Locate and identify every blood parasite.
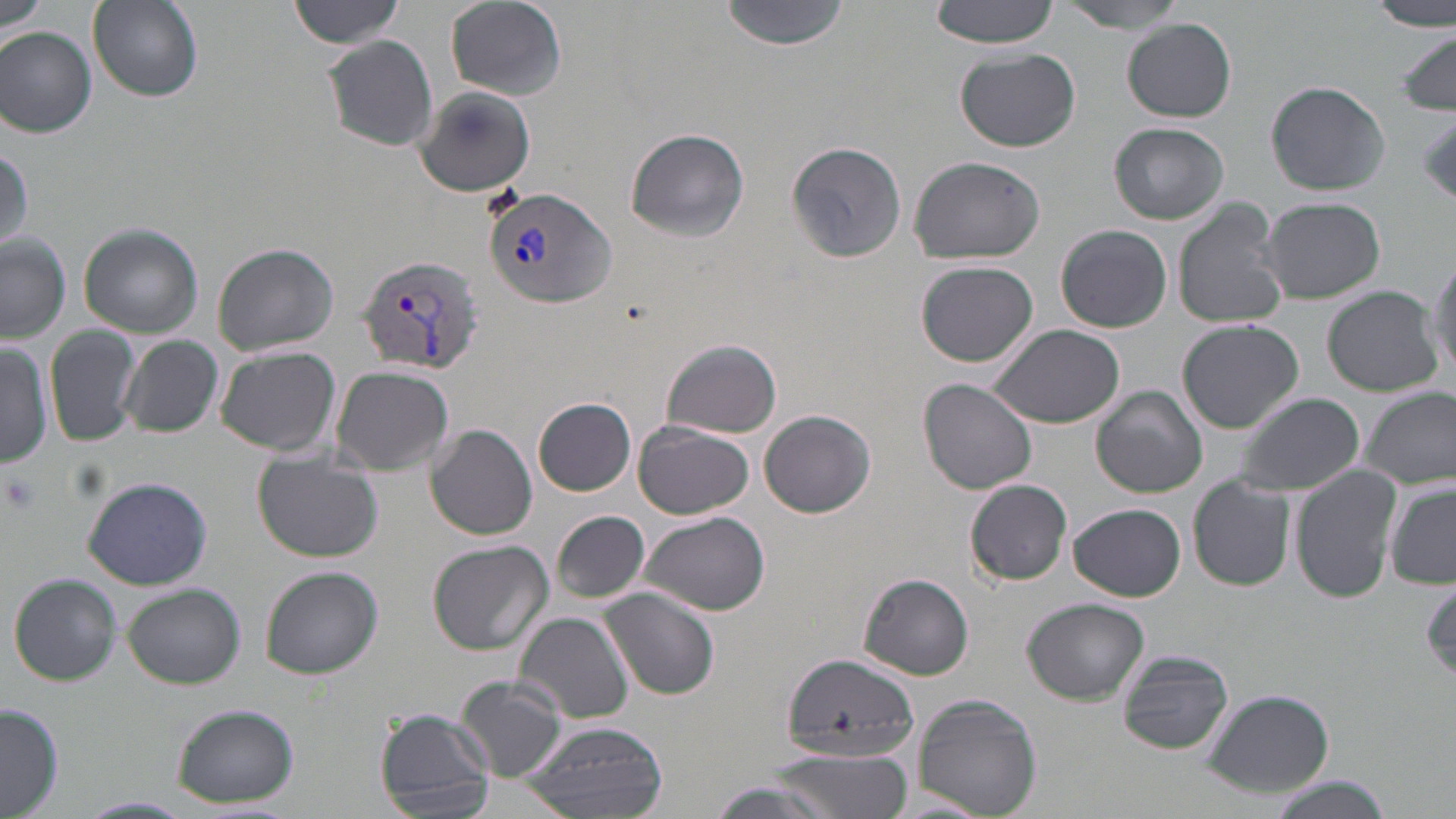
Approximate bounding boxes as (x1,y1)-(x2,y2) corner pairs in pixels.
Plasmodium vivax-infected red blood cells: (483,185)-(617,309), (356,256)-(484,374).
No Plasmodium falciparum, Plasmodium ovale, Plasmodium malariae, Babesia divergens, or Trypanosoma brucei observed.

Summary:
  - Platelet locations: (1417,112)-(1456,206), (1,473)-(40,514)
  - Uninfected red blood cell locations: (288,0)-(407,48), (445,0)-(568,100), (721,0)-(847,52), (927,0)-(1066,48), (1374,0)-(1454,33), (88,1)-(203,103), (1058,1)-(1188,31), (1,2)-(53,39), (1123,19)-(1237,121), (1,27)-(97,137), (1396,30)-(1455,116), (320,35)-(440,153), (955,49)-(1081,152), (1266,80)-(1390,196), (414,86)-(534,198), (1108,123)-(1229,224), (625,128)-(749,242), (784,142)-(916,263), (0,145)-(31,257), (908,155)-(1046,265), (1261,196)-(1386,304), (1171,199)-(1292,329), (78,222)-(204,337), (1055,223)-(1172,333), (0,233)-(71,342), (213,244)-(338,357), (1426,249)-(1455,384), (917,260)-(1039,368), (1323,287)-(1445,396), (1177,319)-(1304,433), (45,325)-(140,447), (991,325)-(1124,429), (119,335)-(224,438), (663,338)-(783,438), (0,342)-(52,468), (215,347)-(341,455), (332,365)-(454,476), (919,380)-(1037,494), (1092,386)-(1208,498), (1362,386)-(1456,491), (1234,392)-(1364,498), (533,398)-(636,495), (760,409)-(876,518), (633,421)-(754,519), (427,425)-(536,541), (252,451)-(383,563), (1290,462)-(1403,605), (82,475)-(213,590), (1188,475)-(1295,591), (966,478)-(1072,585), (1384,483)-(1456,591), (1068,503)-(1187,601), (552,511)-(650,603), (638,511)-(769,616), (427,541)-(554,655), (259,565)-(383,679), (9,573)-(121,686), (857,574)-(975,680), (1421,581)-(1455,687), (121,583)-(245,688), (599,590)-(720,701), (1023,598)-(1149,705), (515,611)-(635,725), (1118,650)-(1233,755), (781,653)-(917,758), (455,674)-(569,782), (1201,687)-(1335,798), (913,694)-(1043,818), (172,703)-(298,808), (0,704)-(64,818), (374,707)-(495,818), (517,720)-(670,817), (764,750)-(914,818), (1265,775)-(1395,819), (701,780)-(849,819), (76,795)-(195,818)
  - Slide-level diagnosis: Plasmodium vivax
  - Image size: 1456×819 pixels
  - Field of view: one of a larger specimen
  - Modality: light microscopy
  - Magnification: 1000x
  - Stain: May-Grünwald-Giemsa
  - Preparation: thin blood smear